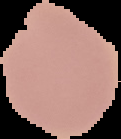
Summary:
  - Result: no Plasmodium parasites seen
  - Image size: 121×139 pixels
  - Preparation: thin blood film
  - Image type: cell region segmented out of the field of view; surrounding area masked to black